Assess this cell for malaria.
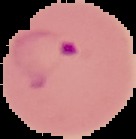
It is parasitized.

Summary:
  - Image type: segmented cell region on a black background
  - Preparation: thin blood smear
  - Image size: 136×139 pixels